Assess for parasitized red blood cells.
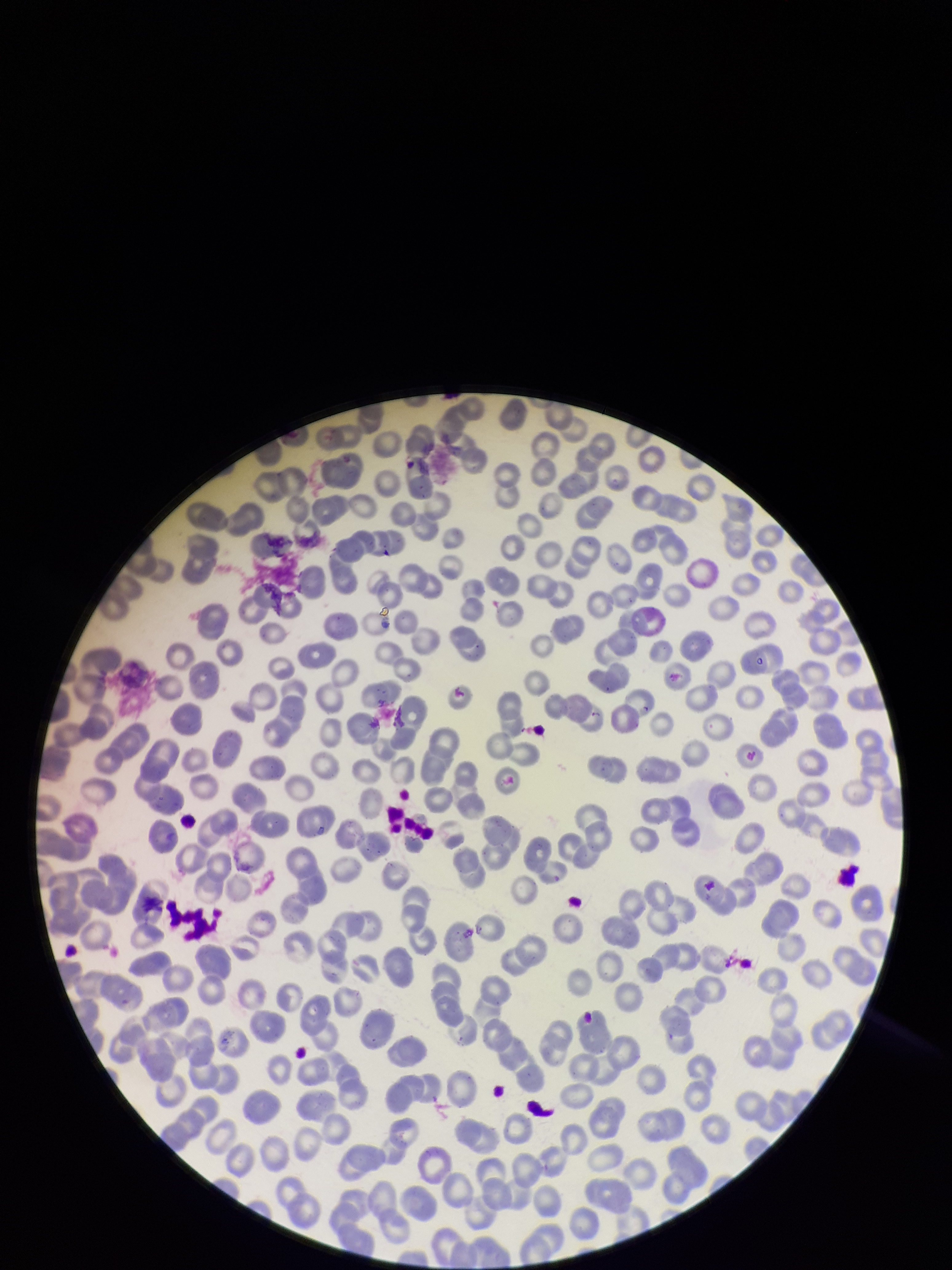

None identified.

patient malaria status = negative
image size = 952×1270 pixels
field of view = one from this slide
parasitized red blood cell count = 0
red blood cell count = 220
stain = Giemsa
preparation = thin
capture = smartphone photograph through the microscope eyepiece